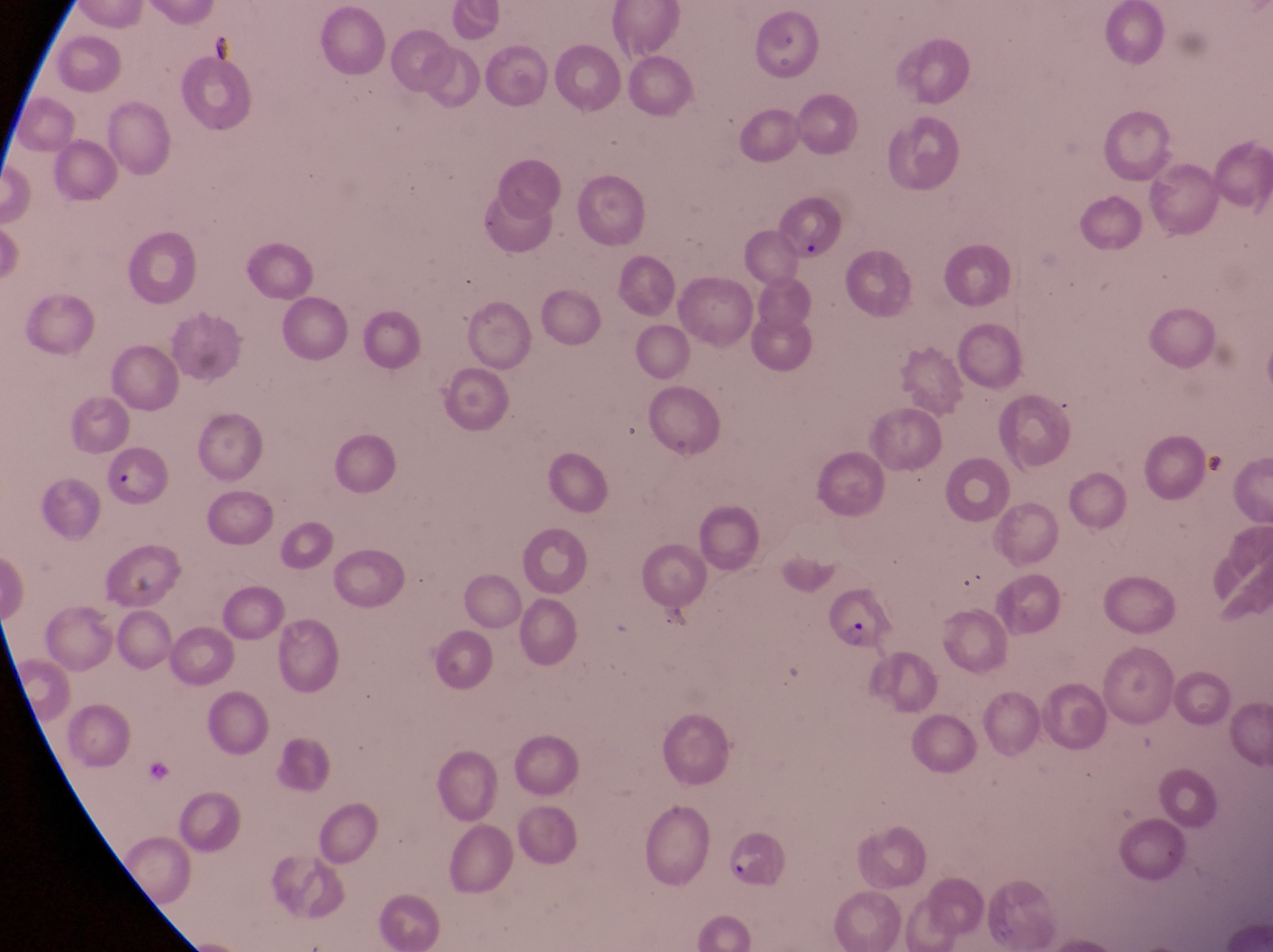

Approximate bounding boxes as {left, top, right, bottom} in pixels. Parasitised red blood cell locations: {102, 444, 174, 509}, {819, 577, 889, 652}, {724, 827, 786, 887}. Photographed through the eyepiece of an Olympus CX-23 microscope with a smartphone camera. Image is 1273×952 pixels. Thin blood film. At a magnification of 1000x. Collected in Uganda. Single field of view.